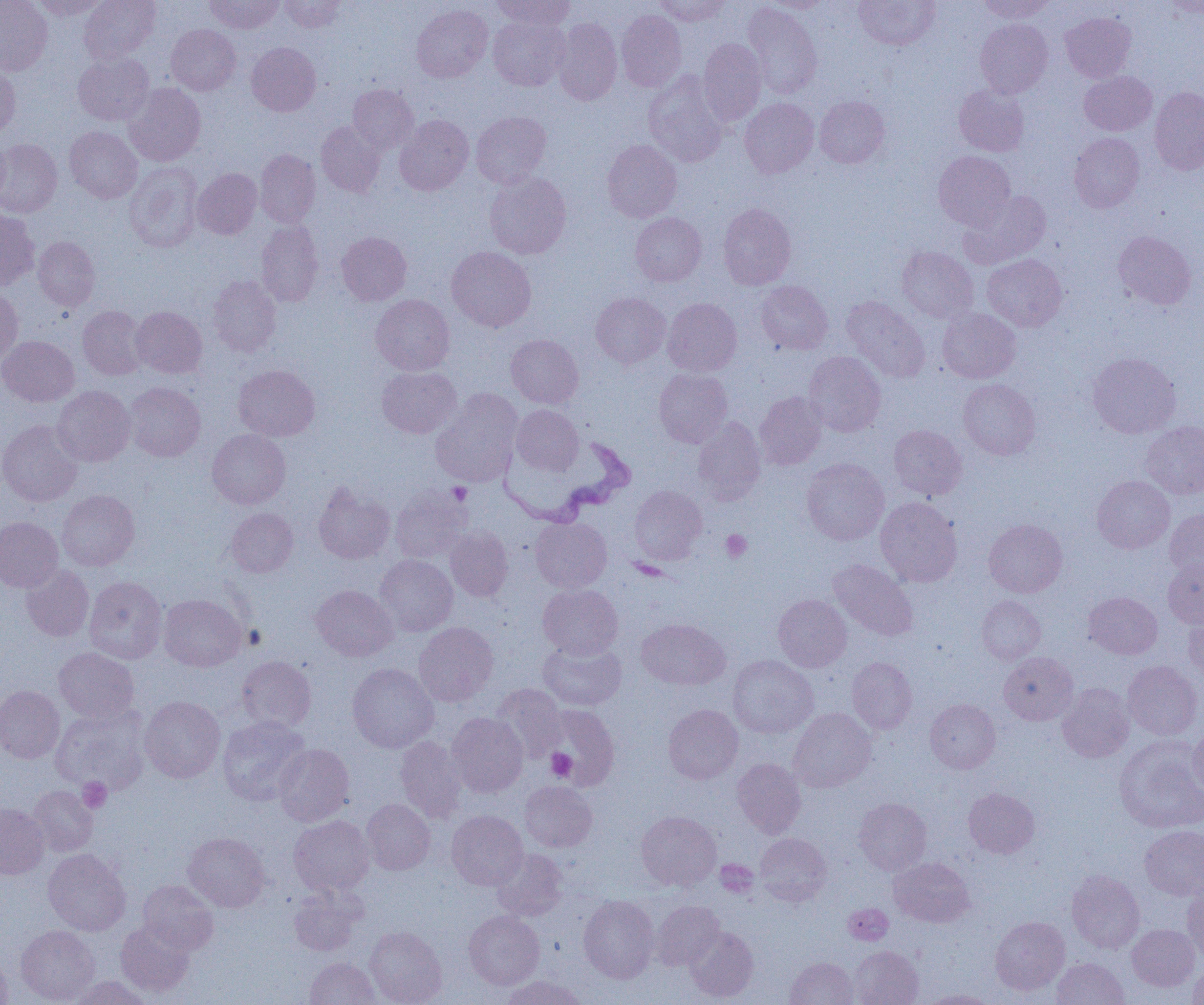 Approximate bounding boxes as (x1,y1)-(x2,y2) corner pairs in pixels. Platelet locations: (447,482)-(472,504), (721,529)-(752,562), (546,749)-(577,780), (78,778)-(111,812), (715,860)-(758,897). Trypanosoma brucei locations: (496,434)-(635,527). Uninfected red blood cell locations: (0,0)-(53,75), (32,0)-(111,19), (79,0)-(160,63), (205,0)-(283,33), (279,0)-(345,32), (492,0)-(575,30), (653,0)-(731,26), (761,0)-(832,12), (854,0)-(940,50), (975,0)-(1054,22), (1163,1)-(1204,19), (743,2)-(822,99), (411,4)-(492,82), (616,10)-(686,91), (1060,12)-(1136,82), (489,17)-(569,90), (552,18)-(622,105), (975,19)-(1053,98), (166,24)-(241,95), (699,38)-(766,125), (247,42)-(321,116), (73,52)-(154,126), (0,63)-(20,139), (643,71)-(728,167), (1080,71)-(1156,135), (124,83)-(206,166), (348,84)-(418,153), (954,84)-(1029,156), (1149,87)-(1204,175), (814,96)-(890,168), (740,98)-(819,178), (471,111)-(551,187), (395,115)-(473,195), (316,121)-(385,197), (65,126)-(142,203), (1069,133)-(1145,212), (0,136)-(9,204), (0,139)-(62,217), (602,140)-(681,222), (255,149)-(320,228), (933,150)-(1015,229), (124,163)-(203,252), (193,169)-(261,239), (484,172)-(571,259), (960,191)-(1051,268), (718,203)-(796,290), (0,209)-(39,291), (630,212)-(706,286), (256,220)-(324,307), (337,231)-(411,305), (1113,231)-(1196,309), (33,236)-(100,311), (447,246)-(536,331), (897,246)-(978,323), (982,254)-(1067,331), (207,275)-(281,356), (756,280)-(833,355), (0,286)-(23,364), (591,292)-(670,367), (371,295)-(454,375), (841,296)-(930,383), (662,298)-(742,376), (78,306)-(148,380), (131,306)-(207,378), (937,308)-(1021,383), (506,334)-(583,408), (0,336)-(79,406), (803,351)-(886,437), (1088,352)-(1181,438), (233,365)-(319,441), (377,366)-(461,438), (654,368)-(733,447), (958,379)-(1040,460), (124,382)-(205,461), (52,386)-(135,466), (431,390)-(522,486), (755,391)-(827,470), (512,405)-(583,475), (692,417)-(766,504), (0,419)-(83,506), (1139,421)-(1204,500), (888,425)-(966,499), (207,429)-(290,509), (802,458)-(889,545), (1092,475)-(1174,553), (313,481)-(395,564), (628,485)-(707,565), (390,486)-(472,563), (57,490)-(139,571), (875,497)-(962,586), (226,507)-(298,577), (1165,509)-(1204,579), (0,516)-(63,592), (531,517)-(612,592), (984,519)-(1067,597), (445,527)-(514,602), (375,555)-(458,636), (1163,558)-(1204,628), (829,559)-(918,641), (21,564)-(94,641), (85,576)-(167,664), (538,584)-(623,658), (311,585)-(398,661), (1084,592)-(1162,659), (159,594)-(247,670), (773,594)-(852,672), (976,596)-(1045,665), (1184,614)-(1204,681), (637,618)-(730,690), (414,622)-(498,706), (537,638)-(626,711), (54,647)-(139,723), (999,652)-(1078,725), (727,655)-(818,738), (237,656)-(316,732), (847,657)-(917,734), (1122,661)-(1202,740), (347,663)-(439,753), (1058,683)-(1134,762), (491,684)-(566,762), (0,685)-(65,763), (140,696)-(225,783), (925,698)-(1000,773), (545,704)-(621,790), (663,704)-(743,784), (51,705)-(151,795), (788,708)-(876,792), (447,712)-(528,797), (217,716)-(311,805), (1188,725)-(1204,798), (395,735)-(468,822), (1114,736)-(1204,834), (273,743)-(354,826), (732,758)-(806,837), (520,781)-(597,852), (29,785)-(97,856), (964,787)-(1040,858), (854,798)-(931,875), (362,799)-(436,874), (0,802)-(49,879), (447,810)-(528,890), (636,810)-(722,890), (289,815)-(374,896), (1140,825)-(1204,899), (183,832)-(270,912), (754,833)-(831,905), (43,848)-(130,936), (491,849)-(568,921), (889,857)-(975,927), (1067,869)-(1145,953), (138,880)-(218,954), (1182,883)-(1204,959), (288,886)-(364,956), (578,895)-(659,983), (652,900)-(724,970), (843,903)-(893,945), (464,910)-(544,989), (990,916)-(1070,994), (115,921)-(195,998), (1127,924)-(1199,990), (16,925)-(99,1004), (365,926)-(447,1005), (685,926)-(759,1002), (849,945)-(923,1005), (0,952)-(12,1004), (305,957)-(380,1005), (786,957)-(858,1005), (1052,958)-(1130,1005), (1188,961)-(1204,1005), (66,976)-(154,1004), (500,976)-(586,1005), (921,989)-(998,1004). Slide-level diagnosis: Trypanosoma brucei. Light microscopy. Captured at 1000x magnification. Thin blood film. One field of a larger specimen. Image is 1204×1005 pixels.